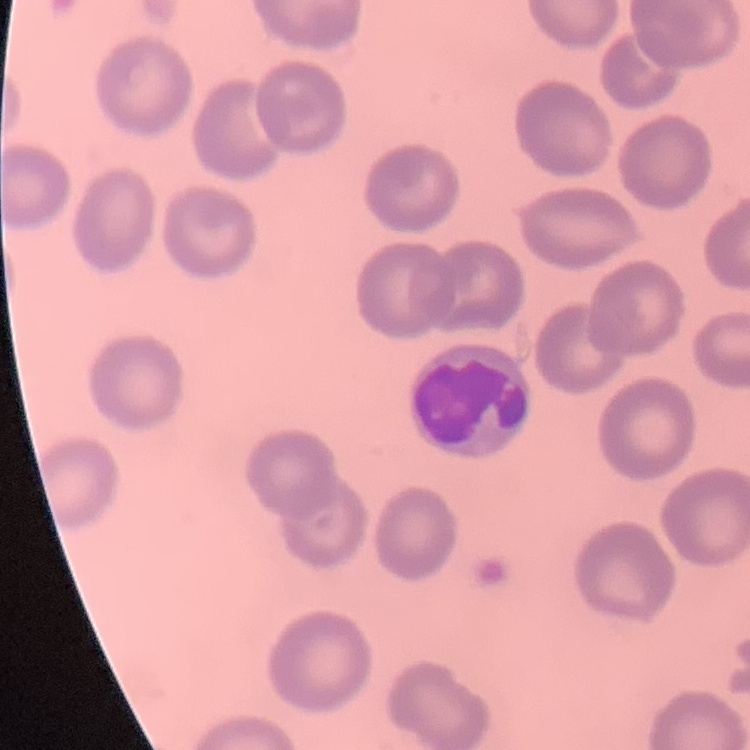 The red blood cells show no rouleaux formation. One tile cut from a larger photomicrograph. Thin peripheral smear. Field's or Giemsa stain.